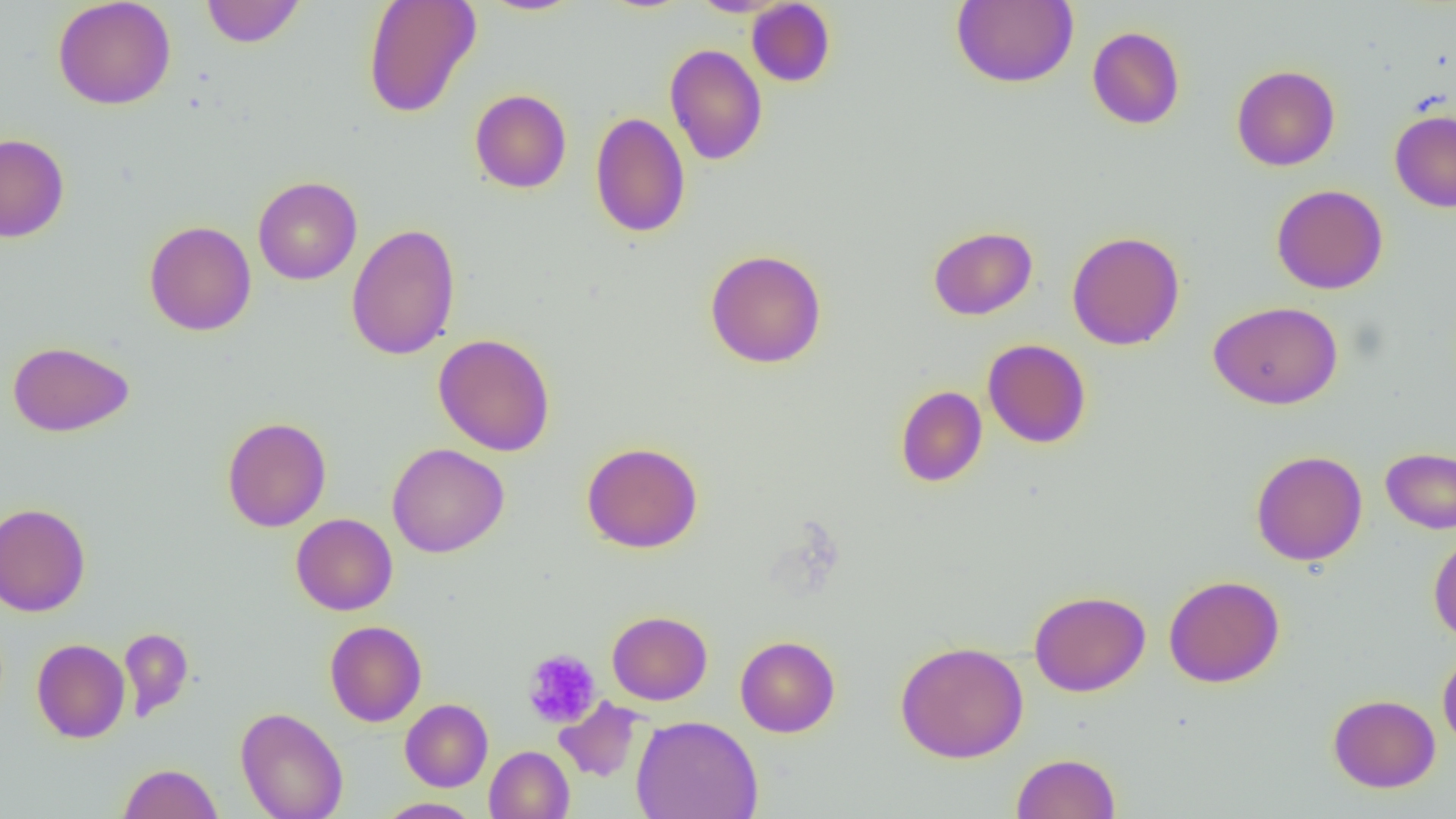

slide-level diagnosis = negative for blood parasites
field of view = single
uninfected red blood cell locations (subset) = approximate bounding boxes as (x1, y1, x2, y2) in pixels: (52, 0, 177, 110), (200, 0, 306, 48), (362, 0, 481, 118), (480, 0, 586, 16), (688, 0, 791, 17), (951, 0, 1079, 88), (746, 1, 836, 87), (1087, 26, 1185, 129), (665, 44, 767, 165), (1231, 65, 1340, 171), (470, 89, 572, 193), (1389, 109, 1456, 212), (589, 111, 690, 238), (0, 134, 69, 243), (253, 176, 362, 285), (1271, 184, 1388, 294), (144, 220, 256, 336), (345, 223, 461, 360), (928, 226, 1037, 320), (1067, 231, 1185, 350), (704, 248, 827, 368), (1208, 301, 1343, 409), (433, 333, 556, 456), (982, 339, 1092, 448), (7, 340, 134, 437), (895, 385, 987, 488), (222, 417, 331, 532), (581, 442, 703, 553), (387, 443, 509, 558), (1381, 448, 1456, 534), (1250, 450, 1367, 566), (0, 502, 91, 617), (291, 513, 398, 615), (1428, 533, 1456, 644), (1164, 575, 1285, 687), (1029, 590, 1151, 696), (607, 610, 712, 705), (324, 620, 427, 726), (119, 627, 194, 722), (735, 635, 840, 737), (31, 638, 130, 743), (895, 640, 1029, 763), (1438, 648, 1456, 754), (1328, 693, 1440, 792), (554, 697, 647, 783), (400, 698, 493, 791), (235, 707, 348, 819), (631, 714, 764, 819), (484, 746, 574, 819), (1011, 752, 1121, 818), (118, 762, 223, 819), (374, 797, 481, 819)
preparation = thin blood smear
modality = light microscopy
image size = 1456×819 pixels
magnification = 1000x